State the blood parasite species.
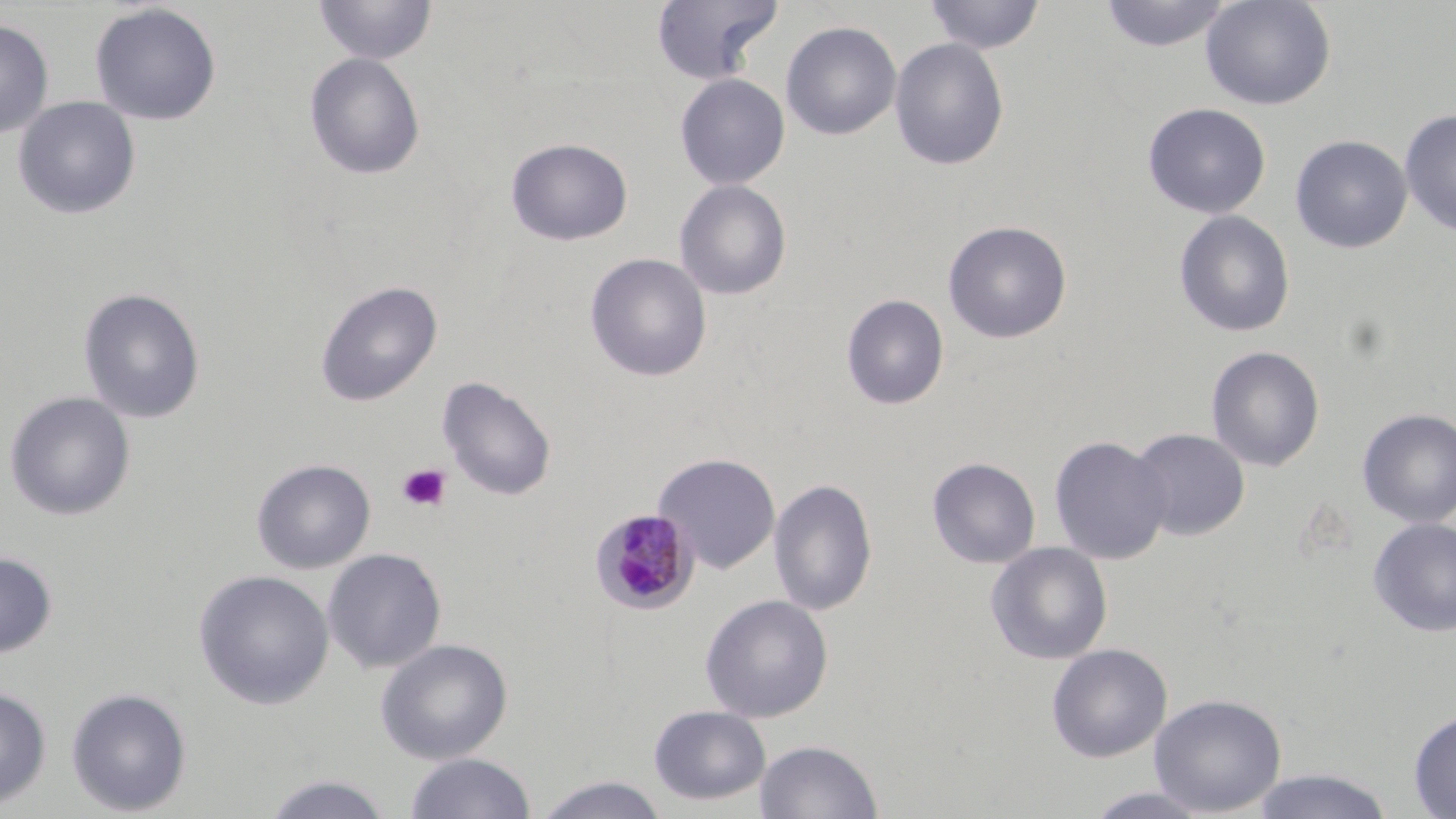

Plasmodium malariae.

Approximate bounding boxes as (x1,y1)-(x2,y2) corner pairs in pixels. Platelet locations: (396,463)-(452,513). Plasmodium malariae-infected red blood cell locations: (589,507)-(699,615). Uninfected red blood cell locations: (314,0)-(437,65), (651,0)-(782,83), (924,0)-(1046,54), (1099,0)-(1232,52), (1201,0)-(1336,111), (90,3)-(221,126), (0,19)-(53,138), (781,21)-(902,140), (889,37)-(1009,171), (304,52)-(426,180), (675,73)-(790,190), (13,97)-(141,220), (1157,102)-(1279,337), (1142,103)-(1271,219), (1399,108)-(1456,236), (1290,135)-(1412,253), (506,138)-(633,246), (674,180)-(792,300), (1173,210)-(1295,338), (943,220)-(1072,343), (585,253)-(712,382), (315,280)-(442,407), (78,288)-(206,424), (841,294)-(949,410), (1206,346)-(1325,472), (437,376)-(557,501), (3,391)-(136,521), (1356,408)-(1456,528), (1128,428)-(1250,541), (1049,435)-(1172,565), (653,452)-(781,574), (927,457)-(1041,569), (251,458)-(376,574), (768,477)-(878,616), (1368,518)-(1456,636), (985,542)-(1113,665), (322,547)-(447,675), (0,552)-(57,658), (193,569)-(334,710), (699,594)-(834,723), (375,638)-(513,764), (1046,643)-(1172,763), (0,684)-(52,810), (65,687)-(193,816), (1149,693)-(1287,816), (648,704)-(770,806), (1408,710)-(1456,818), (755,739)-(883,818), (405,752)-(535,818), (1250,767)-(1395,819), (260,773)-(394,819), (532,775)-(669,819), (1082,787)-(1214,818). Image is 1456×819 pixels. Captured at 1000x magnification. Thin blood smear. May-Grünwald-Giemsa stain. Light microscopy. One field of a larger specimen.